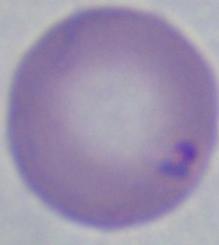
identification = Babesia
magnification = 1000x
modality = photomicrograph